Assess the morphology of the erythrocytes.
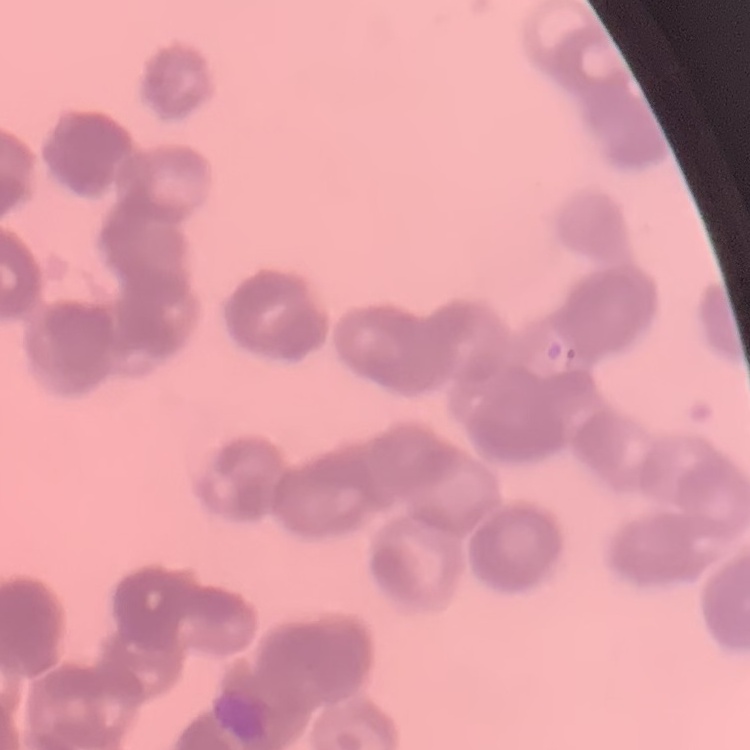

Rouleaux formation.

Stained with either Field's or Giemsa. Thin peripheral smear. One tile cut from a larger photomicrograph.